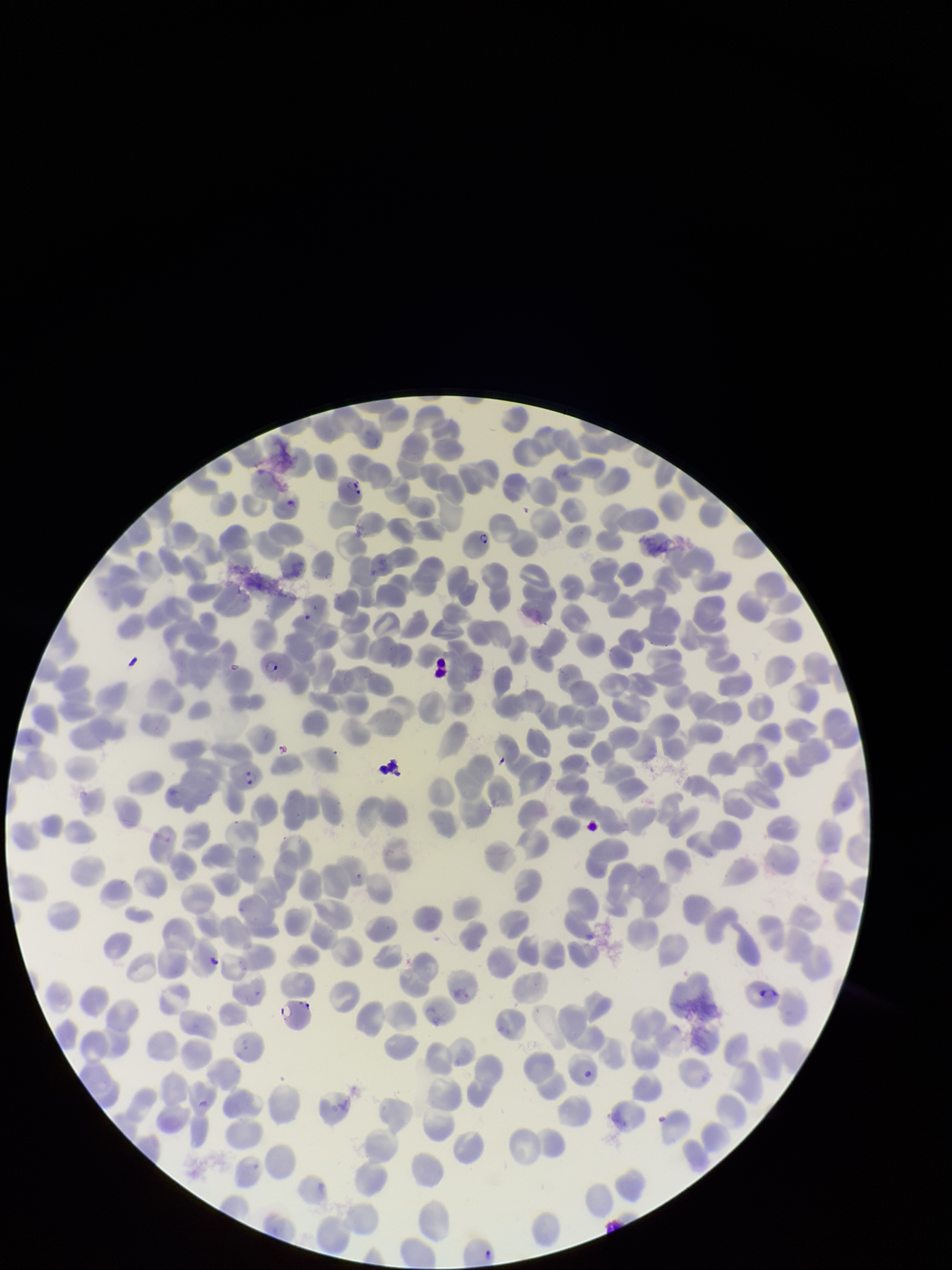

Summary:
  - Stain: Giemsa
  - Species reported for this patient: Plasmodium falciparum
  - Image size: 952×1270 pixels
  - Field of view: one from this slide
  - Parasitized red blood cell count: 7
  - Patient malaria status: positive
  - Preparation: thin blood smear
  - Capture: smartphone photograph through the microscope eyepiece
  - Red blood cell count: 341
  - Parasitized red blood cells: seen